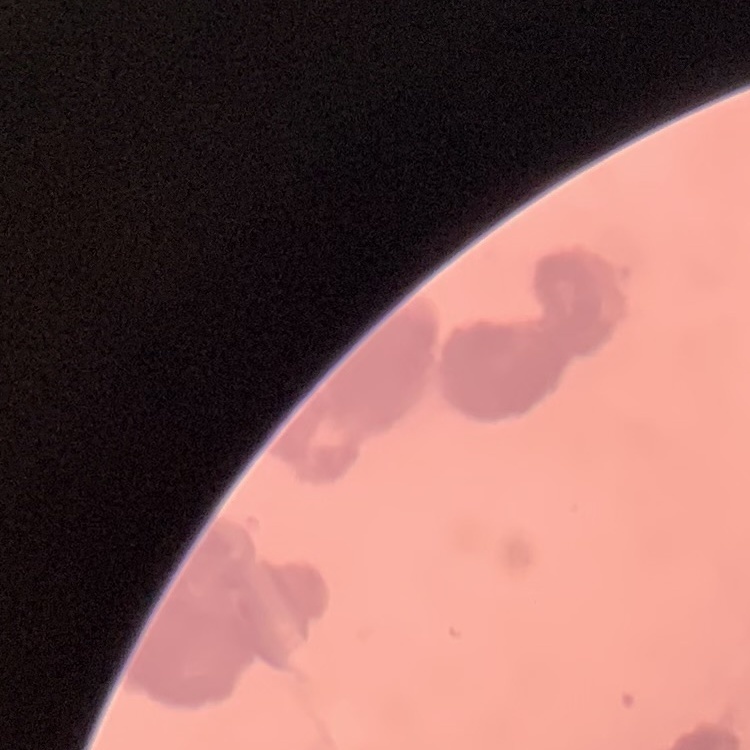

Summary:
  - Red blood cell morphology: rouleaux formation
  - Stain: Field's or Giemsa
  - Preparation: thin blood film
  - Image type: square crop of a larger photomicrograph